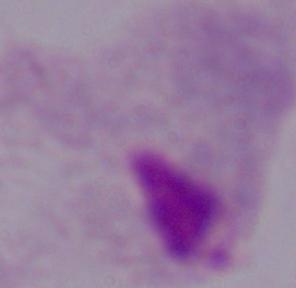

Summary:
  - Magnification: 1000x
  - Identification: trichomonad
  - Modality: photomicrograph